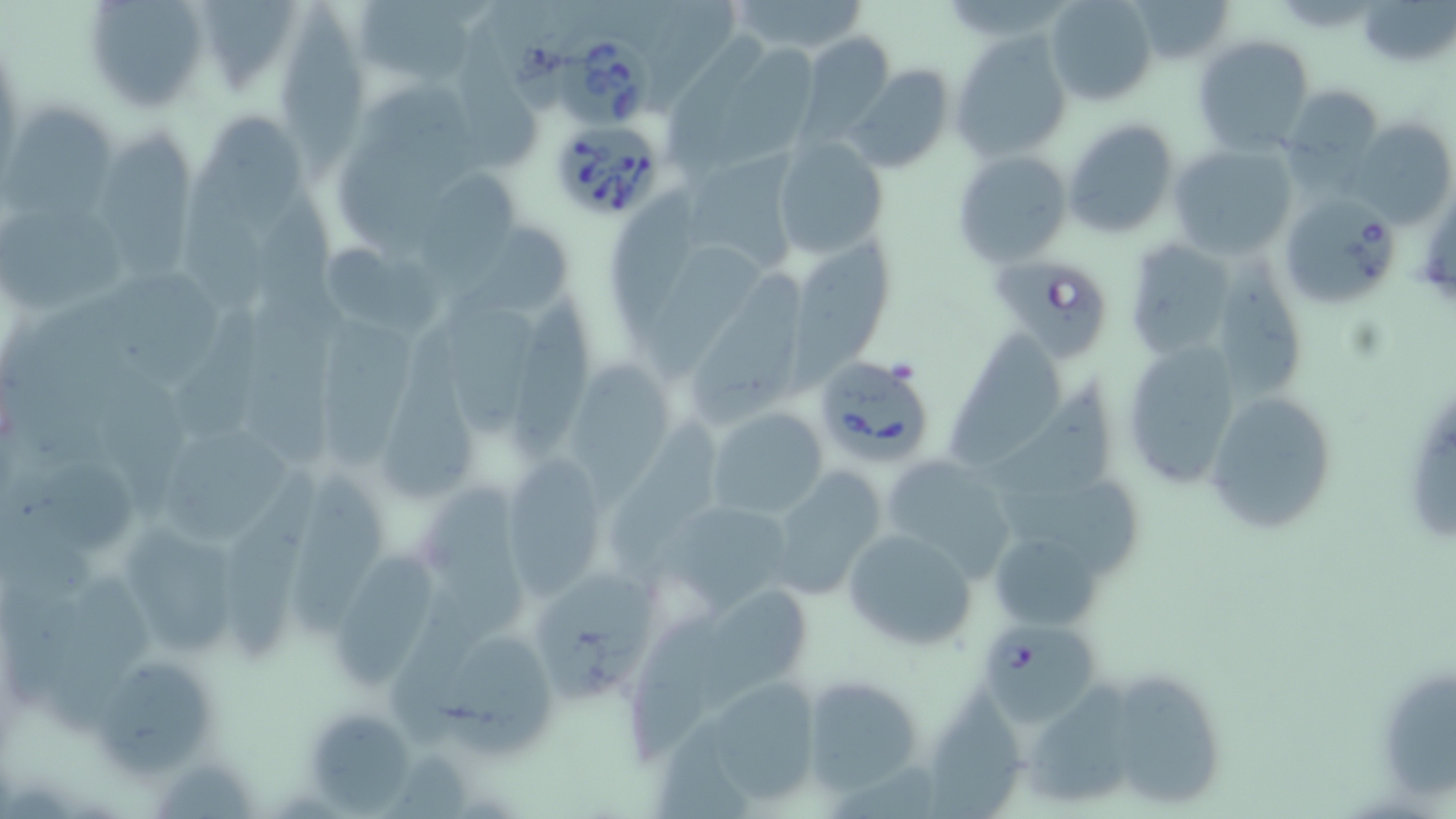
slide_level_diagnosis: Babesia divergens
preparation: thin blood smear
stain: May-Grünwald-Giemsa
field_of_view: single
magnification: 1000x
uninfected_red_blood_cell_locations: 'approximate bounding boxes as (x1, y1, x2, y2) in pixels: (82, 0, 209, 113), (355, 0, 477, 85), (1045, 0, 1158, 106), (1126, 0, 1237, 65), (1358, 0, 1455, 68), (197, 1, 304, 97), (725, 1, 873, 55), (276, 7, 375, 176), (458, 28, 547, 173), (797, 33, 896, 143), (950, 33, 1071, 161), (667, 35, 771, 185), (1194, 35, 1315, 155), (848, 66, 954, 175), (1278, 84, 1386, 186), (8, 104, 114, 215), (202, 110, 304, 241), (1061, 117, 1179, 239), (1348, 119, 1455, 226), (98, 130, 207, 291), (773, 137, 888, 260), (1168, 142, 1297, 258), (685, 145, 804, 272), (951, 150, 1070, 267), (418, 170, 526, 298), (606, 182, 706, 353), (1277, 194, 1401, 309), (2, 208, 132, 314), (460, 228, 580, 319), (1121, 237, 1238, 361), (787, 240, 902, 400), (319, 242, 444, 341), (643, 243, 769, 389), (1218, 253, 1306, 400), (689, 270, 805, 431), (109, 274, 233, 391), (510, 297, 596, 469), (443, 298, 545, 446), (171, 311, 265, 445), (314, 314, 429, 476), (943, 327, 1071, 476), (381, 331, 479, 505), (1119, 339, 1249, 492), (576, 358, 679, 511), (975, 386, 1121, 498), (1203, 389, 1338, 536), (705, 406, 829, 520), (617, 413, 721, 585), (161, 428, 299, 546), (878, 453, 1021, 582), (20, 454, 142, 557), (499, 456, 607, 597), (769, 468, 889, 595), (224, 471, 325, 669), (289, 472, 399, 641), (999, 485, 1149, 576), (430, 493, 531, 634), (667, 507, 793, 615), (841, 526, 979, 651), (126, 530, 249, 654), (992, 537, 1103, 631), (333, 550, 449, 693), (536, 576, 656, 694), (40, 581, 158, 740), (701, 585, 814, 719), (399, 593, 480, 754), (623, 611, 726, 771), (445, 632, 559, 762), (103, 665, 215, 777), (1382, 672, 1456, 796), (1113, 674, 1225, 806), (799, 675, 927, 796), (702, 679, 827, 806), (1029, 683, 1138, 801), (927, 689, 1021, 814), (309, 714, 421, 816)'
modality: light microscopy
babesia_divergens_infected_red_blood_cell_locations: 'approximate bounding boxes as (x1, y1, x2, y2) in pixels: (560, 35, 658, 127), (547, 116, 666, 223), (995, 260, 1107, 361), (810, 353, 938, 471), (984, 624, 1106, 731)'
image_size: 1456×819 pixels